Point out each malaria parasite.
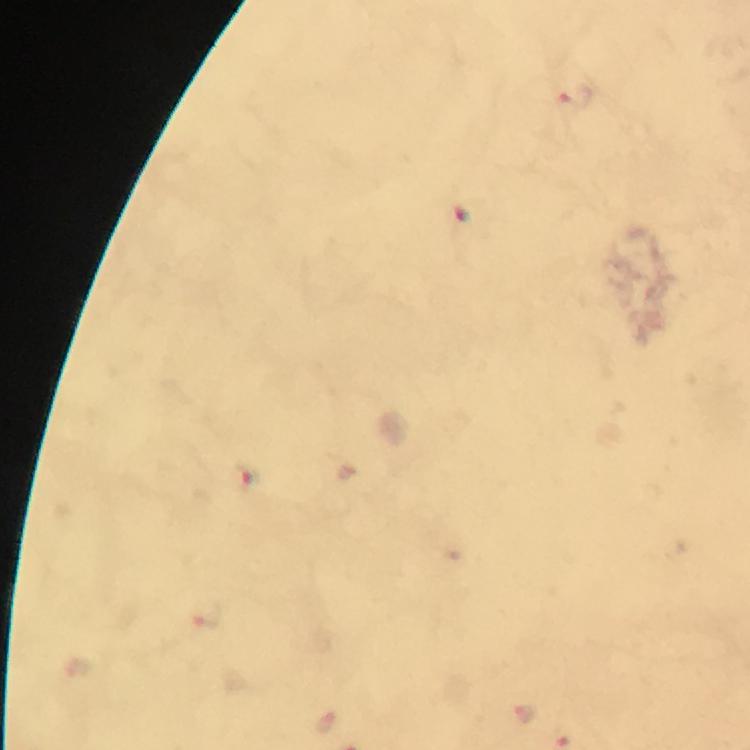
Approximate object centers, in pixels from the top-left corner.
Malaria parasites: (x=577, y=95), (x=467, y=217), (x=244, y=478).

100x magnification. Image is 750×750 pixels. Photographed through the microscope with a smartphone camera. From a diagnostic examination for malaria. Giemsa stain. A crop from one field of view. Immersion oil was used. Thick blood smear.